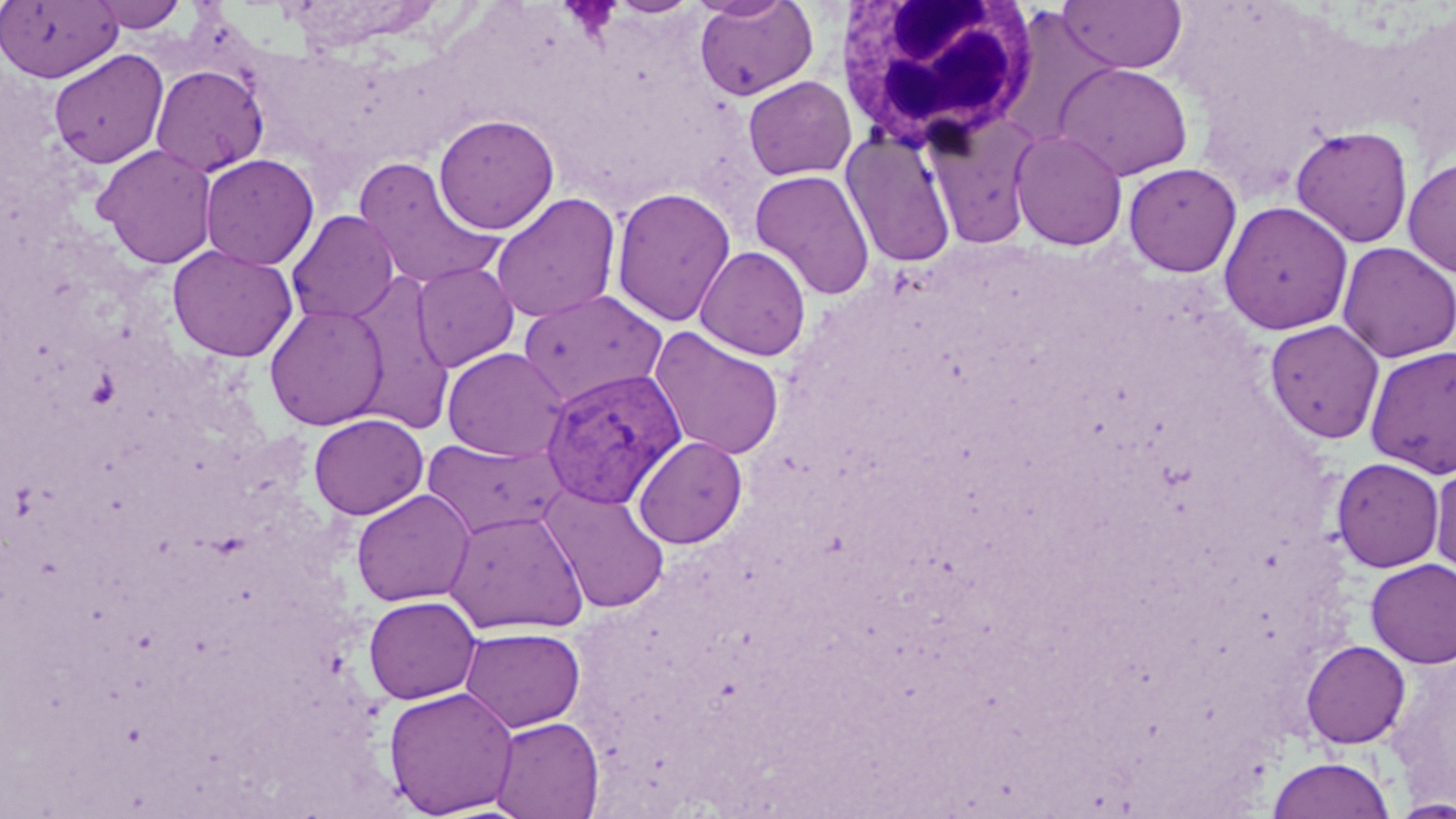
slide_level_diagnosis: Plasmodium vivax
white_blood_cell_locations: 'approximate bounding boxes as (x1,y1)-(x2,y2) corner pairs in pixels: (832,0)-(1041,154)'
image_size: 1456×819 pixels
plasmodium_vivax_infected_red_blood_cell_locations: 'approximate bounding boxes as (x1,y1)-(x2,y2) corner pairs in pixels: (538,367)-(684,510)'
magnification: 1000x
preparation: thin blood smear
modality: light microscopy
field_of_view: one of a larger specimen
stain: May-Grünwald-Giemsa
uninfected_red_blood_cell_locations: 'approximate bounding boxes as (x1,y1)-(x2,y2) corner pairs in pixels: (89,0)-(189,32), (1056,0)-(1187,74), (0,1)-(122,83), (693,1)-(819,101), (49,49)-(168,168), (1054,62)-(1193,180), (151,64)-(269,177), (742,76)-(856,181), (923,112)-(1042,251), (433,114)-(559,235), (1291,125)-(1414,247), (842,129)-(957,268), (1010,129)-(1128,250), (94,144)-(218,269), (200,154)-(319,271), (1402,157)-(1456,278), (353,158)-(504,292), (1123,162)-(1241,276), (749,169)-(876,300), (610,186)-(736,327), (491,193)-(621,324), (1218,201)-(1354,335), (287,210)-(399,325), (1337,241)-(1456,363), (167,244)-(298,362), (695,245)-(812,361), (411,262)-(520,372), (347,274)-(455,433), (517,289)-(669,407), (264,303)-(389,431), (1264,319)-(1385,444), (648,326)-(785,461), (1364,345)-(1456,478), (441,347)-(569,462), (308,413)-(429,520), (632,435)-(748,548), (421,436)-(568,539), (1331,457)-(1445,572), (1430,461)-(1456,581), (539,485)-(671,613), (351,489)-(475,607), (444,508)-(588,635), (1366,558)-(1456,667), (363,595)-(482,704), (460,626)-(586,732), (1301,640)-(1411,748), (383,686)-(519,817), (489,716)-(605,819), (1267,755)-(1396,819), (1388,797)-(1456,818)'